Give the position of every malaria parasite.
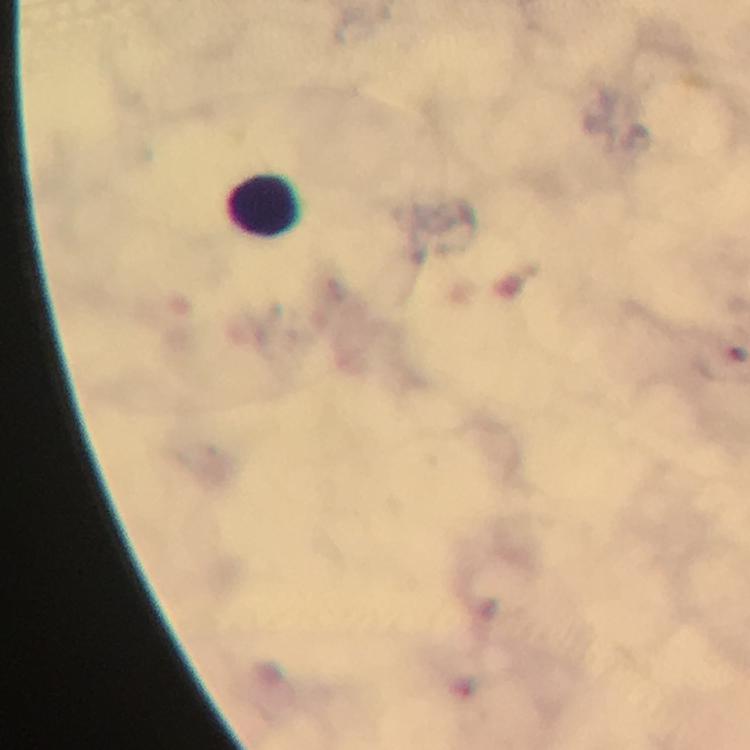
No malaria parasites detected.

cropped from = one field of view
capture = smartphone camera through the microscope
immersion oil = used
leukocyte locations = approximate centers as (x, y) in pixels: (268, 208)
image size = 750×750 pixels
context = from a diagnostic examination for malaria
magnification = 100x
stain = Giemsa
preparation = thick blood smear